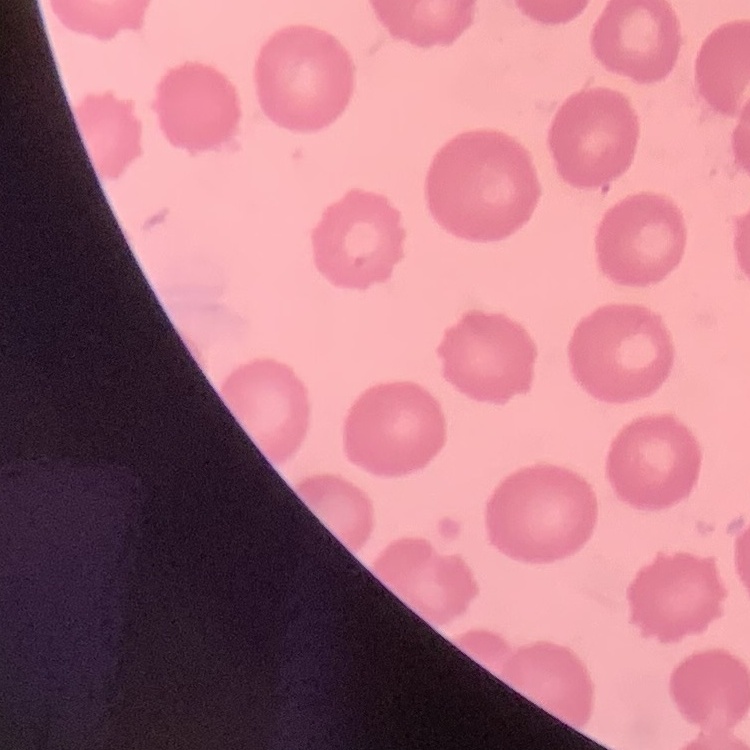

Summary:
  - Red blood cell morphology: no rouleaux formation
  - Stain: Field's or Giemsa
  - Image type: one tile cut from a larger photomicrograph
  - Preparation: thin blood smear